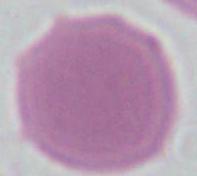

1000x magnification. A red blood cell is shown. Micrograph.